Locate every leukocyte (white blood cell).
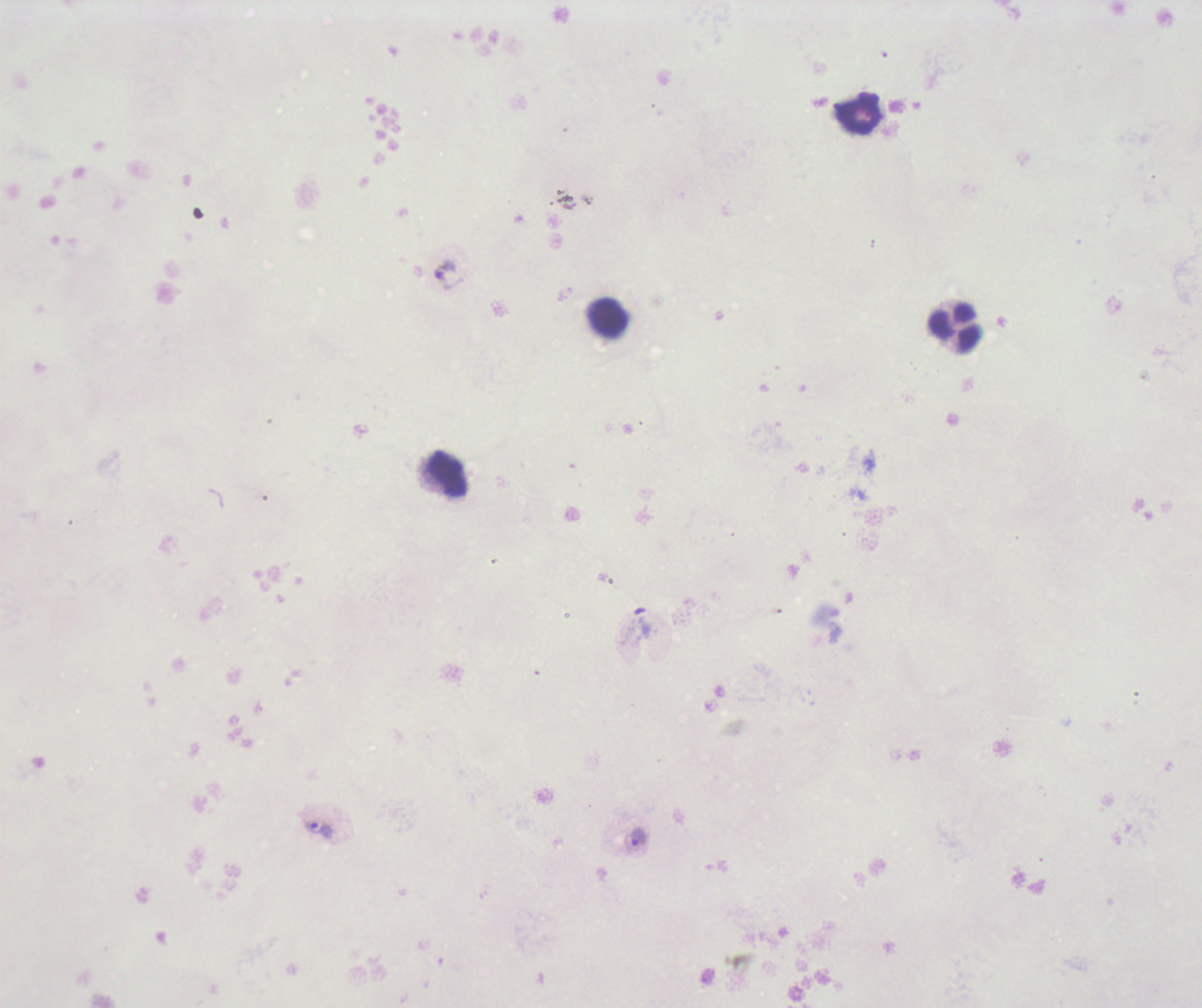

Approximate centers as (x, y) in pixels.
Leukocytes: (861, 114), (607, 318), (954, 327), (447, 474).

Approximate centers as (x, y) in pixels. Trophozoite locations: (448, 274), (318, 830), (637, 838). Previously used in a real diagnosis. Result: Plasmodium parasites detected. Romanowsky stain. Coloration quality: bad. 100x magnification. One field from this slide. Background quality: poor. Thick smear of blood. Image is 1202×1008 pixels.